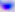
Toxoplasma gondii is seen. 400x magnification. Photomicrograph.